Report the malaria status of this cell.
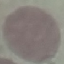
Uninfected.

Summary:
  - Image type: automatically extracted cell patch, resized to 64 × 64 pixels
  - Stain: Giemsa
  - Preparation: thin blood smear
  - Capture: smartphone through the microscope eyepiece